State the blood parasite species.
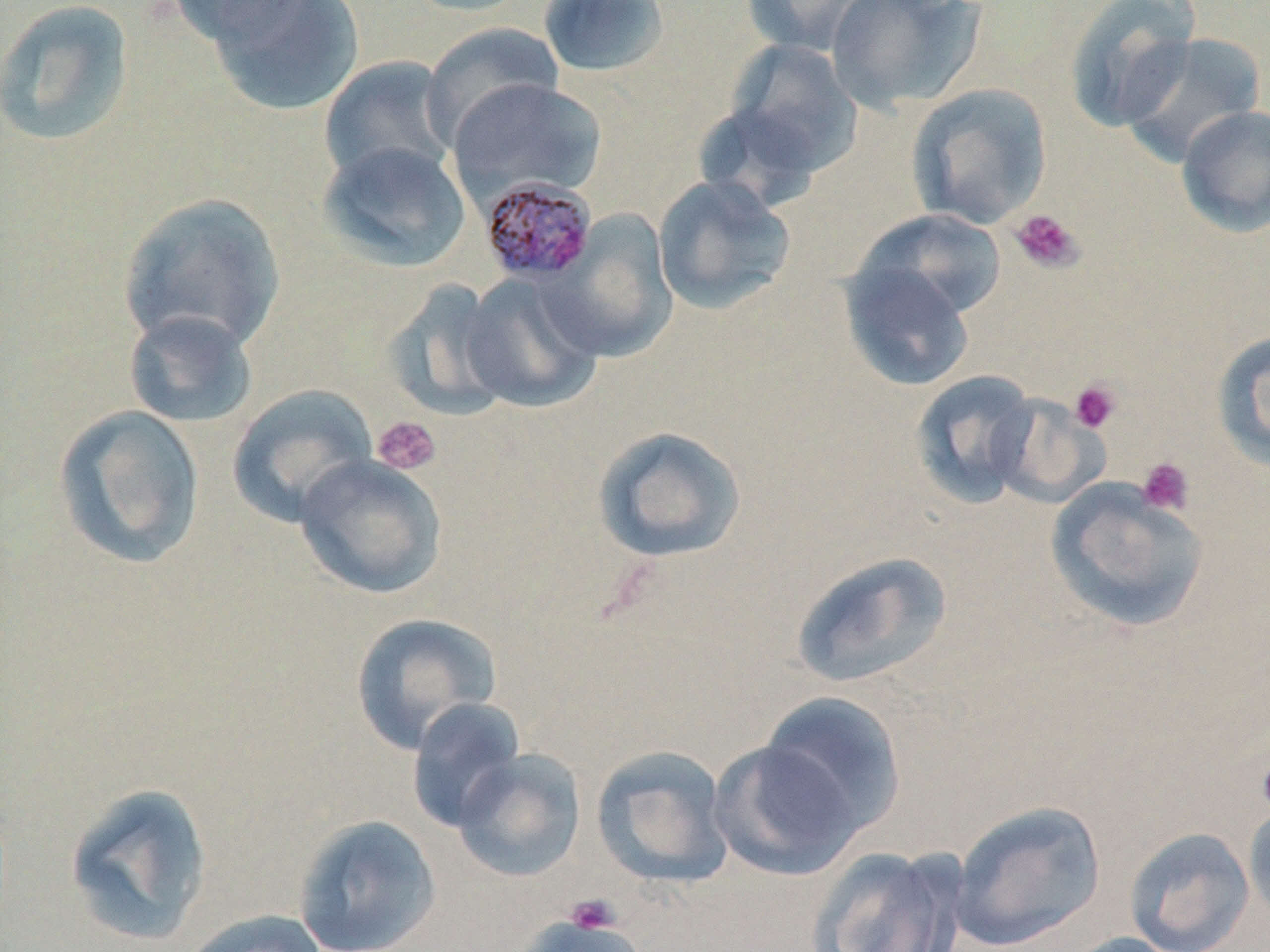
Plasmodium malariae.

Approximate bounding boxes as (x1,y1)-(x2,y2) corner pairs in pixels. Plasmodium malariae-infected red blood cell locations: (480,174)-(600,284). Platelet locations: (1008,208)-(1084,274), (1069,379)-(1122,434), (371,416)-(442,477), (1137,457)-(1195,516), (1256,746)-(1270,821), (565,894)-(621,937). Uninfected red blood cell locations: (0,0)-(136,147), (164,0)-(309,48), (202,0)-(365,116), (398,0)-(535,17), (741,0)-(879,57), (825,0)-(986,113), (1062,0)-(1200,132), (538,1)-(671,78), (421,22)-(564,147), (1118,32)-(1266,167), (723,40)-(862,177), (319,55)-(460,187), (446,78)-(607,204), (906,82)-(1052,230), (1175,104)-(1270,238), (317,140)-(472,273), (653,174)-(796,315), (117,191)-(287,353), (856,208)-(1008,321), (542,210)-(678,362), (839,259)-(975,392), (460,271)-(604,414), (382,278)-(517,422), (123,309)-(259,429), (1211,329)-(1270,472), (909,369)-(1041,510), (227,384)-(378,528), (989,393)-(1109,509), (53,403)-(206,569), (592,425)-(748,565), (293,454)-(448,600), (1045,479)-(1211,633), (790,550)-(953,690), (349,612)-(502,755), (758,691)-(907,838), (406,697)-(527,833), (710,738)-(864,880), (590,745)-(735,889), (452,748)-(587,883), (64,781)-(213,947), (947,800)-(1106,950), (1243,802)-(1270,930), (292,814)-(442,952), (1124,827)-(1255,952), (805,845)-(968,952), (179,909)-(330,952), (515,912)-(642,952), (1055,932)-(1186,952). May-Grünwald-Giemsa-stained preparation. Captured at 1000x magnification. Thin blood film. Image is 1270×952 pixels. Single field of view. Light microscopy.